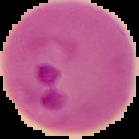 Image is 139×139 pixels. Result: malaria parasites identified. Cell region segmented out of the field of view; the surrounding area is masked to black. From a thin blood smear.